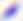
Summary:
  - Magnification: 400x
  - Modality: micrograph
  - Identification: Toxoplasma gondii